Classify this cell by malaria status.
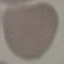
It is uninfected.

capture: smartphone camera at the microscope eyepiece
stain: Giemsa
preparation: thin blood smear
image_type: cell patch, automatically extracted from a larger field of view and resized to 64 × 64 pixels